Give the position of every P. falciparum parasite, noting its life-cycle stage.
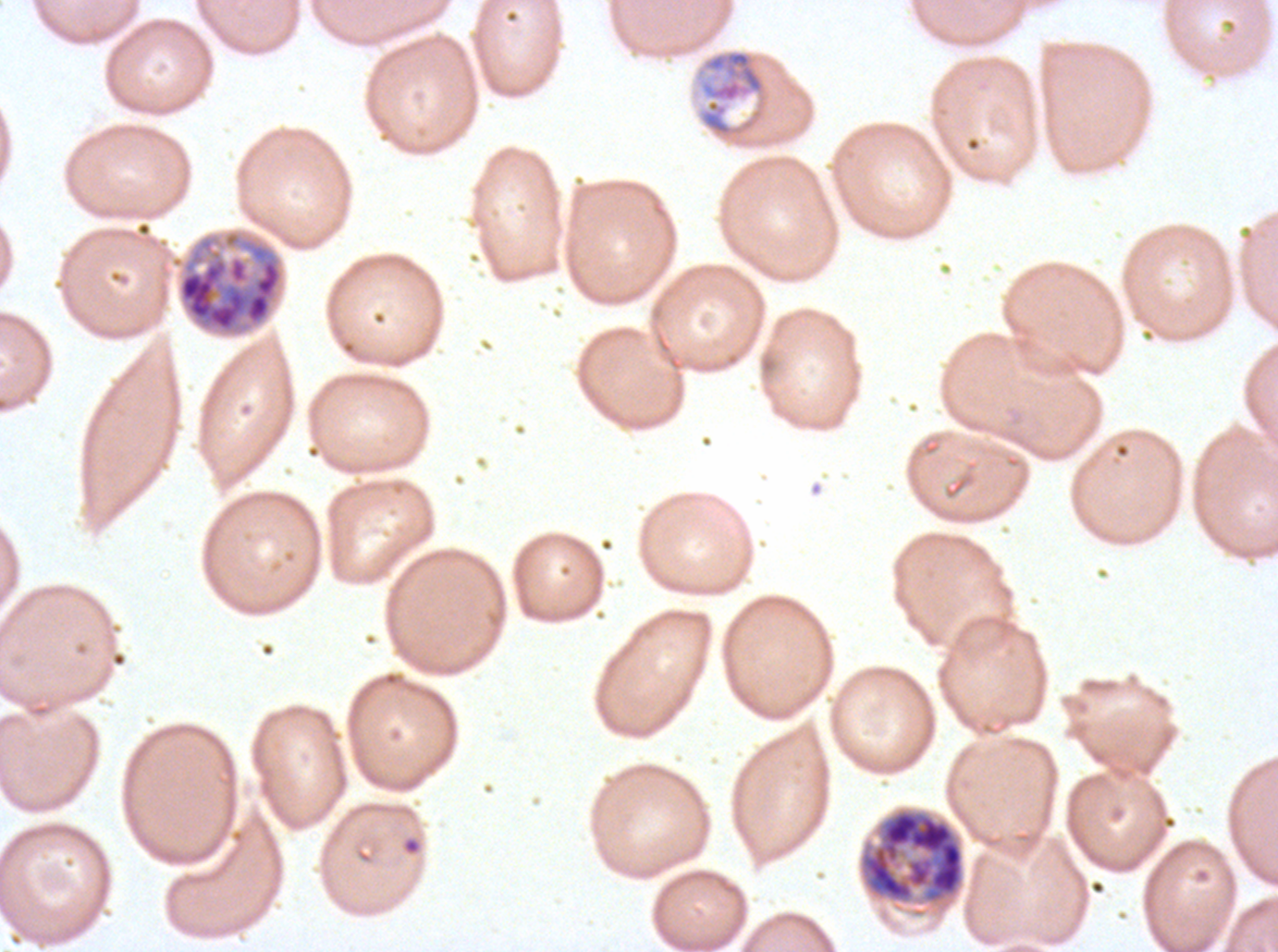

Approximate bounding boxes as {x1, y1, x2, y2} in pixels.
Mid trophozoites: {697, 48, 769, 143}.
Early schizonts: {857, 805, 966, 919}.
Late schizonts: {170, 228, 286, 338}.
No rings, late-ring/early-trophozoite forms, late trophozoites, segmenters, or gametocytes observed.

debris locations = {401, 836, 422, 856}
preparation = thin blood smear
life-cycle stages observed = mid trophozoite, early schizont, late schizont
stain = Giemsa
image size = 1278×952 pixels
specimen = ex-vivo P. falciparum culture from a patient in The Gambia, grown for 24 to 48 hours
field of view = sub-image separated from a larger composite